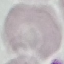

Malaria status: uninfected. Photographed with a smartphone camera at the microscope eyepiece. Thin smear of blood. Cell patch, automatically extracted from a larger field of view and resized to 64 × 64 pixels. Giemsa-stained preparation.